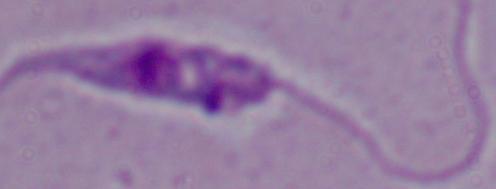

magnification: 1000x
identification: Leishmania
modality: micrograph